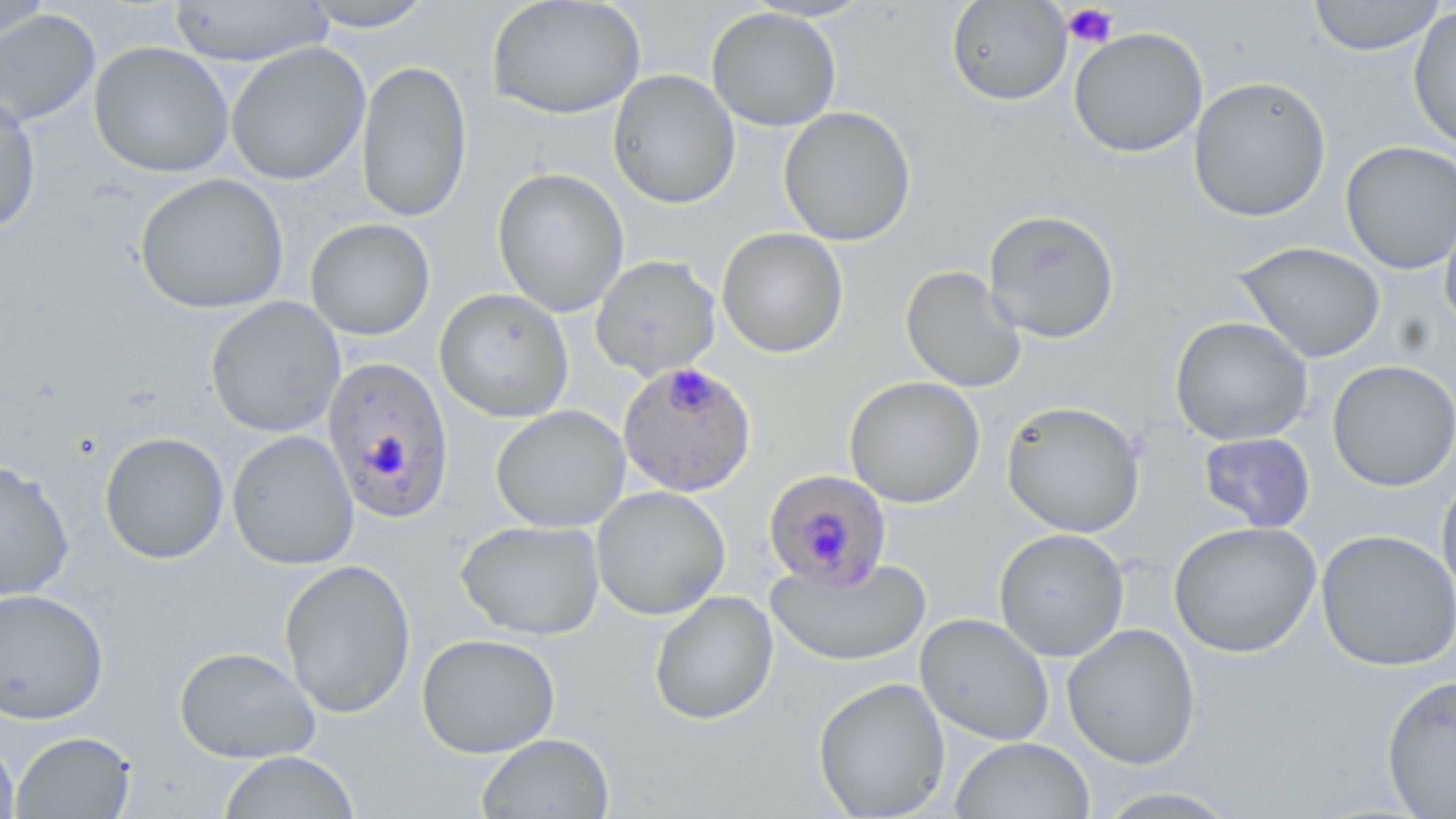

Approximate bounding boxes as (x1,y1)-(x2,y2) corner pairs in pixels. Plasmodium falciparum-infected red blood cell locations: (321,355)-(455,524), (617,361)-(757,498), (763,469)-(893,590). Uninfected red blood cell locations: (1,0)-(50,58), (168,0)-(334,67), (486,0)-(647,120), (945,0)-(1073,106), (1306,0)-(1446,56), (298,1)-(437,32), (706,6)-(842,132), (1407,6)-(1456,152), (0,8)-(100,128), (1068,27)-(1208,158), (89,41)-(235,178), (225,42)-(371,186), (356,59)-(473,223), (607,69)-(741,210), (1187,76)-(1332,223), (0,92)-(42,234), (778,106)-(917,247), (1340,141)-(1456,275), (492,167)-(630,317), (134,173)-(290,314), (1440,202)-(1456,334), (982,208)-(1121,344), (305,218)-(436,341), (716,228)-(849,359), (1232,241)-(1386,364), (590,255)-(721,379), (900,265)-(1027,393), (434,288)-(574,423), (205,296)-(345,439), (1169,316)-(1314,446), (1326,359)-(1456,492), (843,376)-(985,508), (1001,400)-(1145,538), (491,405)-(630,533), (226,430)-(359,570), (99,431)-(229,565), (1198,432)-(1316,532), (0,460)-(74,601), (1436,474)-(1456,604), (591,486)-(731,620), (455,519)-(605,640), (1168,520)-(1321,658), (992,527)-(1130,662), (1315,529)-(1456,672), (765,556)-(932,668), (278,559)-(416,719), (0,588)-(109,724), (648,591)-(779,726), (915,613)-(1055,746), (1061,622)-(1201,770), (415,633)-(561,759), (174,645)-(320,764), (1380,673)-(1456,818), (812,677)-(951,818), (11,730)-(137,819), (476,732)-(615,818), (0,734)-(19,819), (949,737)-(1094,818), (218,751)-(360,818), (1089,786)-(1245,818). Platelet locations: (1062,4)-(1118,48). Slide-level diagnosis: Plasmodium falciparum. May-Grünwald-Giemsa-stained preparation. Single field of view. Image is 1456×819 pixels. Optical microscopy. 1000x magnification. Thin blood film.